Report the malaria status of this cell.
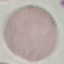

Uninfected.

Summary:
  - Capture: smartphone through the microscope eyepiece
  - Preparation: thin blood film
  - Stain: Giemsa
  - Image type: cell patch, automatically extracted from a larger field of view and resized to 64 × 64 pixels